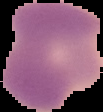

Summary:
  - Result: Plasmodium parasites detected
  - Preparation: thin blood film
  - Image type: segmented cell region with the area outside set to black
  - Image size: 103×112 pixels